Name the cell type shown.
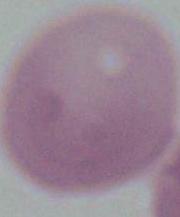

An erythrocyte.

Captured at 1000x magnification. Photomicrograph.